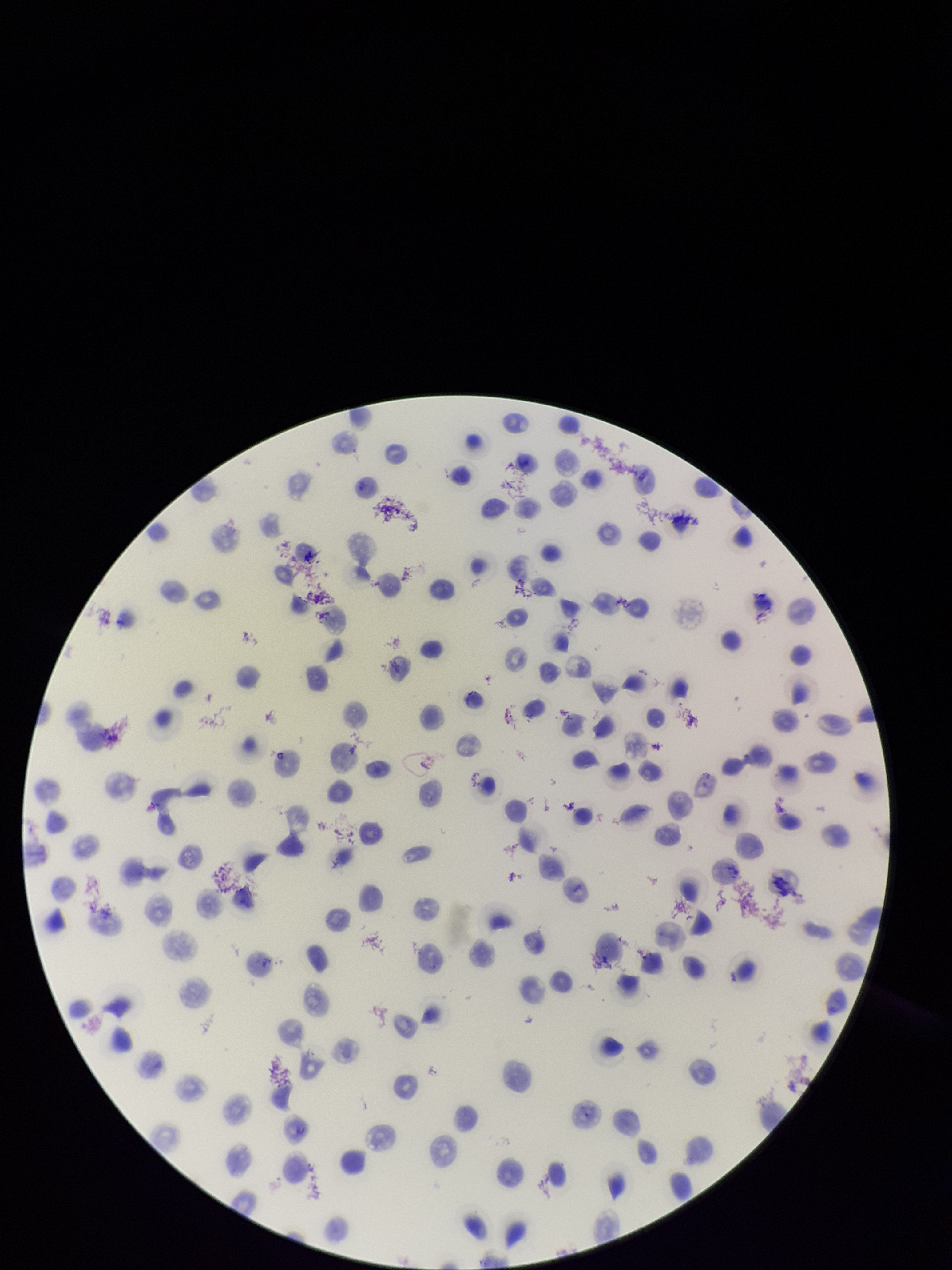
Parasitized red blood cell count: 0. Preparation: thin smear. Single field of view. Parasitized red blood cells: none detected. Stained with Giemsa. Image is 952×1270 pixels. Smartphone photograph taken through the eyepiece of a microscope. Red blood cell count: 133. Species reported for this patient: Plasmodium vivax. Patient malaria status: positive.